Describe the morphology of the erythrocytes.
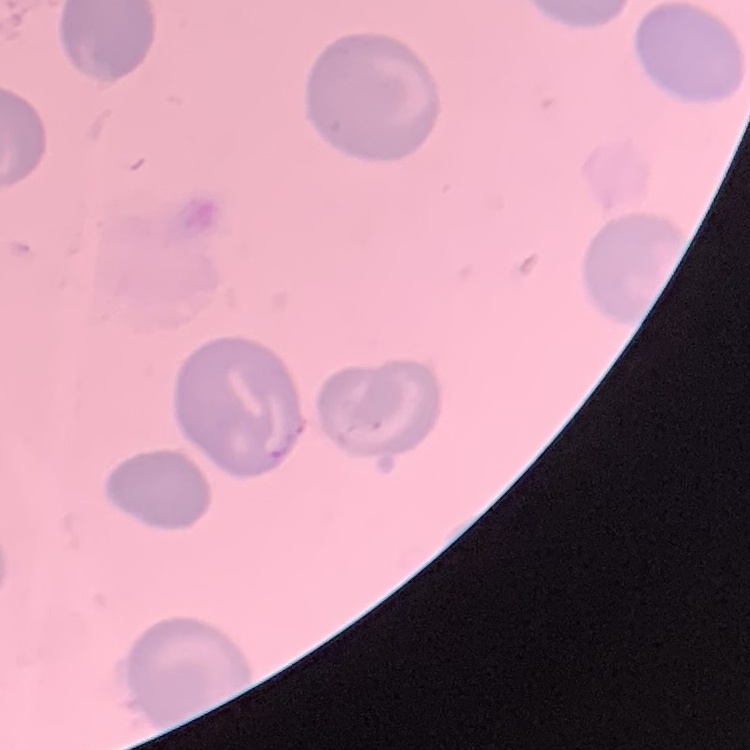
They show no rouleaux formation.

Thin blood smear. Stained with either Field's or Giemsa. Square crop of a larger photomicrograph.